Outline platelets.
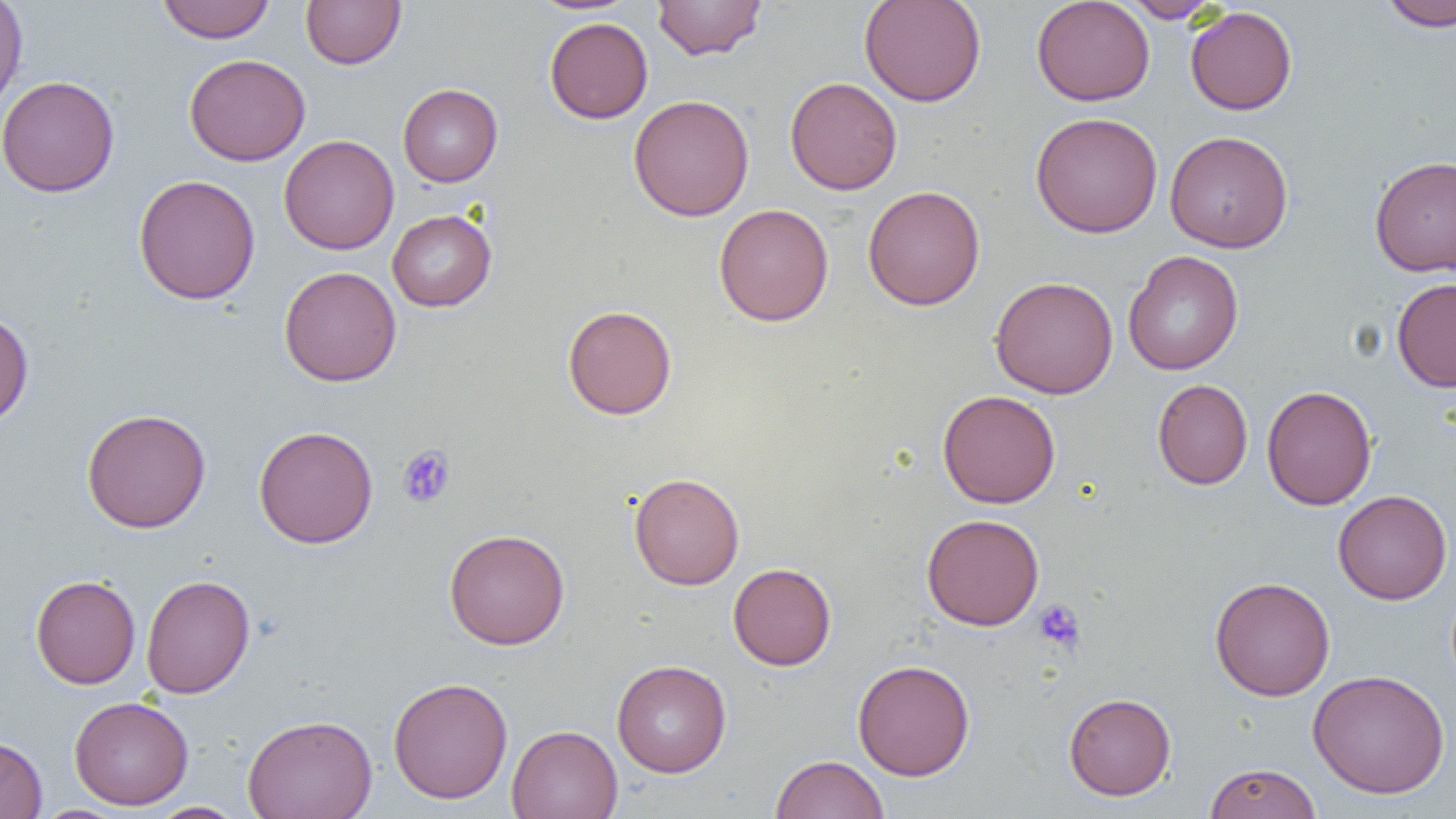

Approximate bounding boxes as named x1/y1/x2/y2 corners in pixels.
Platelets: (x1=396, y1=445, x2=456, y2=509), (x1=1033, y1=599, x2=1086, y2=653).

Summary:
  - Uninfected red blood cell locations: (x1=0, y1=0, x2=28, y2=114), (x1=157, y1=0, x2=275, y2=44), (x1=301, y1=0, x2=406, y2=69), (x1=652, y1=0, x2=767, y2=60), (x1=859, y1=0, x2=987, y2=107), (x1=1031, y1=0, x2=1155, y2=106), (x1=1120, y1=0, x2=1223, y2=23), (x1=1378, y1=0, x2=1456, y2=32), (x1=1185, y1=6, x2=1298, y2=115), (x1=544, y1=17, x2=653, y2=124), (x1=184, y1=53, x2=311, y2=166), (x1=0, y1=75, x2=119, y2=197), (x1=785, y1=77, x2=902, y2=195), (x1=398, y1=83, x2=503, y2=186), (x1=628, y1=94, x2=755, y2=221), (x1=1030, y1=111, x2=1163, y2=238), (x1=1164, y1=130, x2=1293, y2=253), (x1=279, y1=134, x2=399, y2=254), (x1=1369, y1=154, x2=1456, y2=277), (x1=133, y1=174, x2=261, y2=305), (x1=862, y1=185, x2=985, y2=310), (x1=714, y1=203, x2=834, y2=326), (x1=387, y1=209, x2=497, y2=312), (x1=1122, y1=250, x2=1243, y2=375), (x1=279, y1=266, x2=402, y2=387), (x1=990, y1=276, x2=1119, y2=399), (x1=1391, y1=278, x2=1456, y2=392), (x1=562, y1=304, x2=677, y2=419), (x1=0, y1=310, x2=34, y2=428), (x1=1152, y1=379, x2=1253, y2=489), (x1=1261, y1=385, x2=1377, y2=510), (x1=937, y1=390, x2=1060, y2=508), (x1=82, y1=408, x2=211, y2=533), (x1=254, y1=425, x2=378, y2=548), (x1=629, y1=472, x2=745, y2=590), (x1=1333, y1=489, x2=1452, y2=605), (x1=922, y1=514, x2=1044, y2=631), (x1=444, y1=529, x2=570, y2=650), (x1=728, y1=563, x2=836, y2=670), (x1=140, y1=574, x2=255, y2=698), (x1=31, y1=575, x2=140, y2=689), (x1=1210, y1=576, x2=1335, y2=701), (x1=852, y1=659, x2=976, y2=780), (x1=612, y1=660, x2=731, y2=777), (x1=1307, y1=669, x2=1450, y2=799), (x1=388, y1=677, x2=513, y2=803), (x1=1063, y1=692, x2=1176, y2=800), (x1=69, y1=695, x2=193, y2=809), (x1=242, y1=713, x2=377, y2=819), (x1=507, y1=725, x2=623, y2=819), (x1=0, y1=735, x2=47, y2=819), (x1=770, y1=754, x2=889, y2=819), (x1=1203, y1=762, x2=1322, y2=819), (x1=147, y1=802, x2=247, y2=818), (x1=32, y1=805, x2=128, y2=819)
  - Slide-level diagnosis: no evidence of blood parasites
  - Field of view: single
  - Magnification: 1000x
  - Modality: optical microscopy
  - Preparation: thin blood smear
  - Image size: 1456×819 pixels